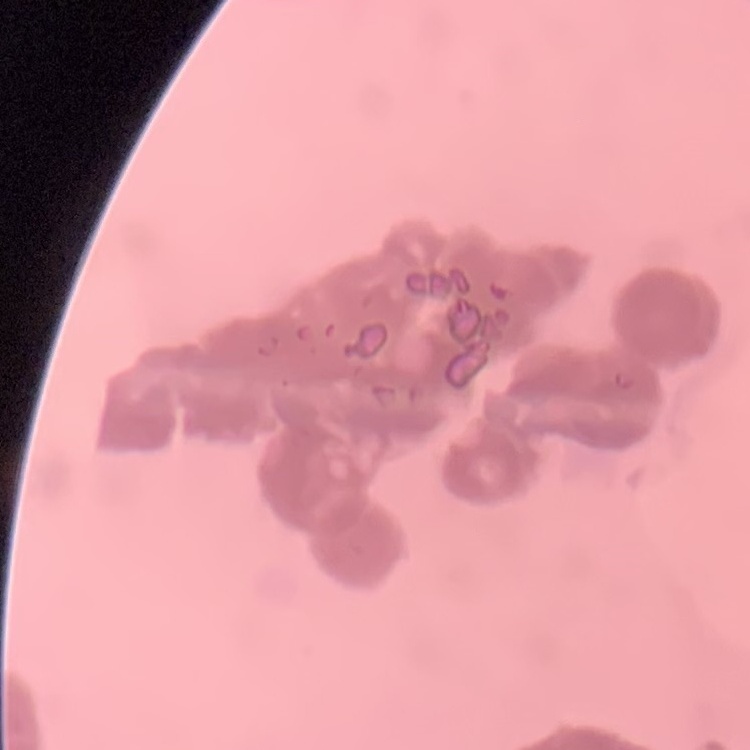

The erythrocytes exhibit rouleaux formation. Square crop of a larger photomicrograph. Field's or Giemsa stain. Thin blood film.